Identify the parasite.
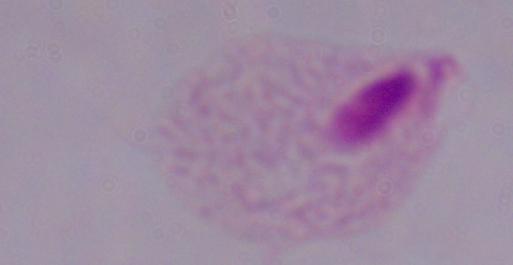
A trichomonad.

Summary:
  - Magnification: 1000x
  - Modality: micrograph